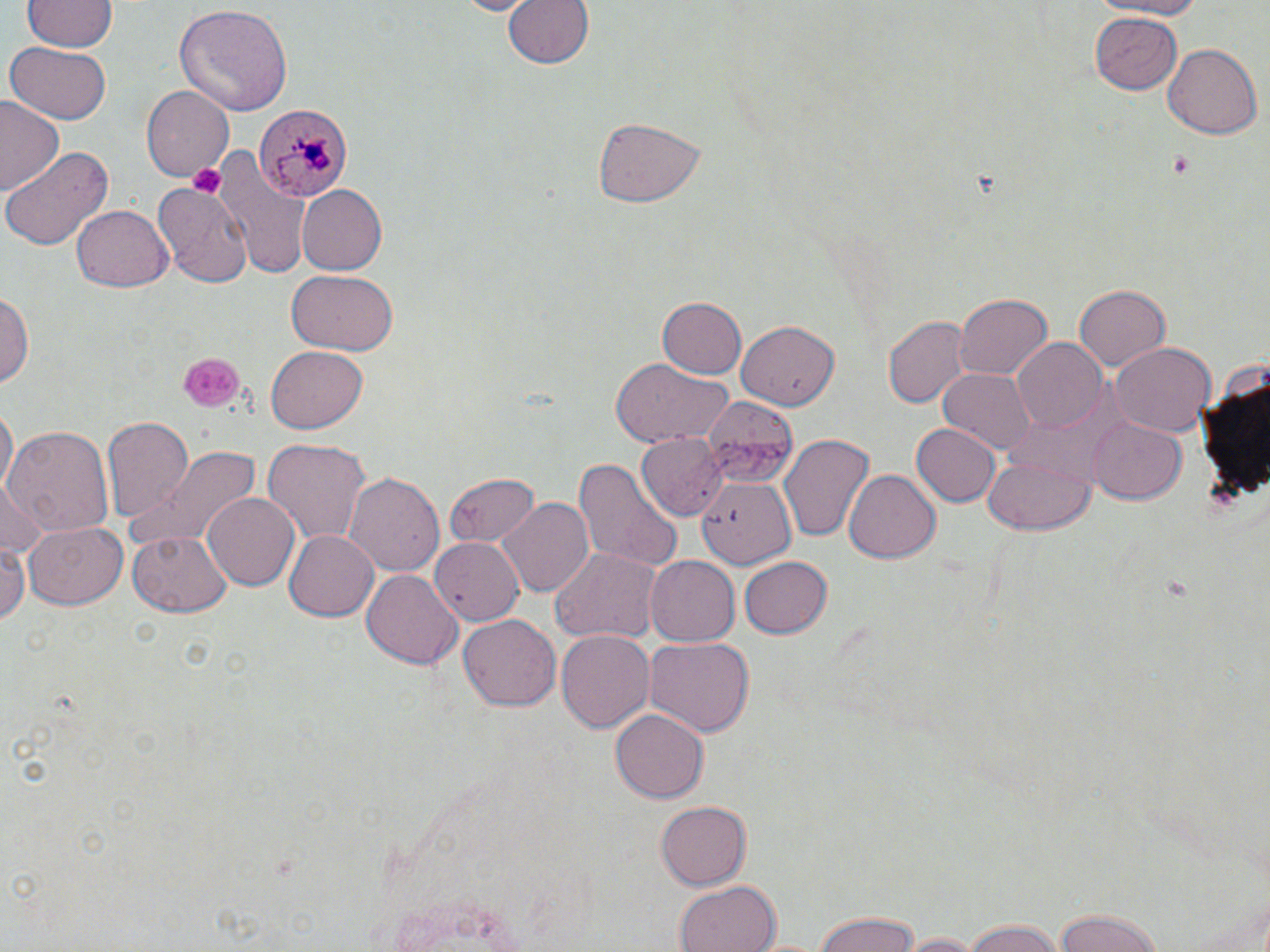
Approximate bounding boxes as (x1, y1, x2, y2) in pixels. Uninfected red blood cell locations: (502, 0, 593, 71), (1091, 0, 1214, 18), (22, 1, 116, 54), (175, 5, 292, 117), (1090, 12, 1184, 95), (3, 43, 113, 125), (1163, 43, 1261, 140), (141, 85, 235, 180), (0, 97, 64, 197), (590, 115, 707, 208), (2, 145, 115, 250), (210, 145, 312, 280), (154, 178, 251, 287), (296, 185, 388, 276), (72, 204, 170, 290), (286, 268, 399, 355), (1072, 285, 1169, 372), (1, 289, 34, 391), (955, 293, 1054, 379), (656, 297, 747, 379), (883, 313, 970, 411), (737, 316, 840, 407), (1010, 338, 1109, 435), (1111, 342, 1216, 437), (263, 346, 369, 436), (610, 356, 731, 447), (938, 367, 1036, 456), (701, 397, 798, 483), (1, 406, 17, 498), (100, 412, 195, 524), (1087, 414, 1187, 502), (911, 423, 1000, 506), (4, 426, 114, 542), (776, 432, 876, 545), (637, 434, 728, 520), (262, 437, 371, 546), (130, 444, 261, 549), (983, 454, 1095, 535), (576, 457, 682, 574), (844, 468, 941, 564), (344, 471, 443, 578), (444, 474, 540, 547), (694, 476, 793, 567), (0, 480, 47, 558), (200, 490, 299, 590), (499, 496, 594, 598), (22, 521, 125, 609), (283, 528, 379, 622), (128, 530, 232, 617), (431, 536, 523, 627), (0, 541, 28, 627), (551, 544, 661, 643), (644, 555, 739, 646), (738, 555, 831, 638), (362, 571, 463, 670), (458, 615, 561, 712), (556, 630, 654, 732), (644, 636, 755, 739), (610, 708, 707, 803), (654, 802, 753, 889), (674, 879, 782, 952), (1052, 909, 1171, 952), (812, 910, 924, 952), (959, 919, 1068, 952), (896, 931, 987, 951). Plasmodium malariae-infected red blood cell locations: (251, 103, 354, 202). Platelet locations: (1168, 153, 1193, 174), (188, 161, 227, 198), (178, 353, 244, 412). Slide-level diagnosis: Plasmodium malariae. 1000x magnification. One field of a larger specimen. May-Grünwald-Giemsa stain. Image is 1270×952 pixels. Optical microscopy. Thin blood film.